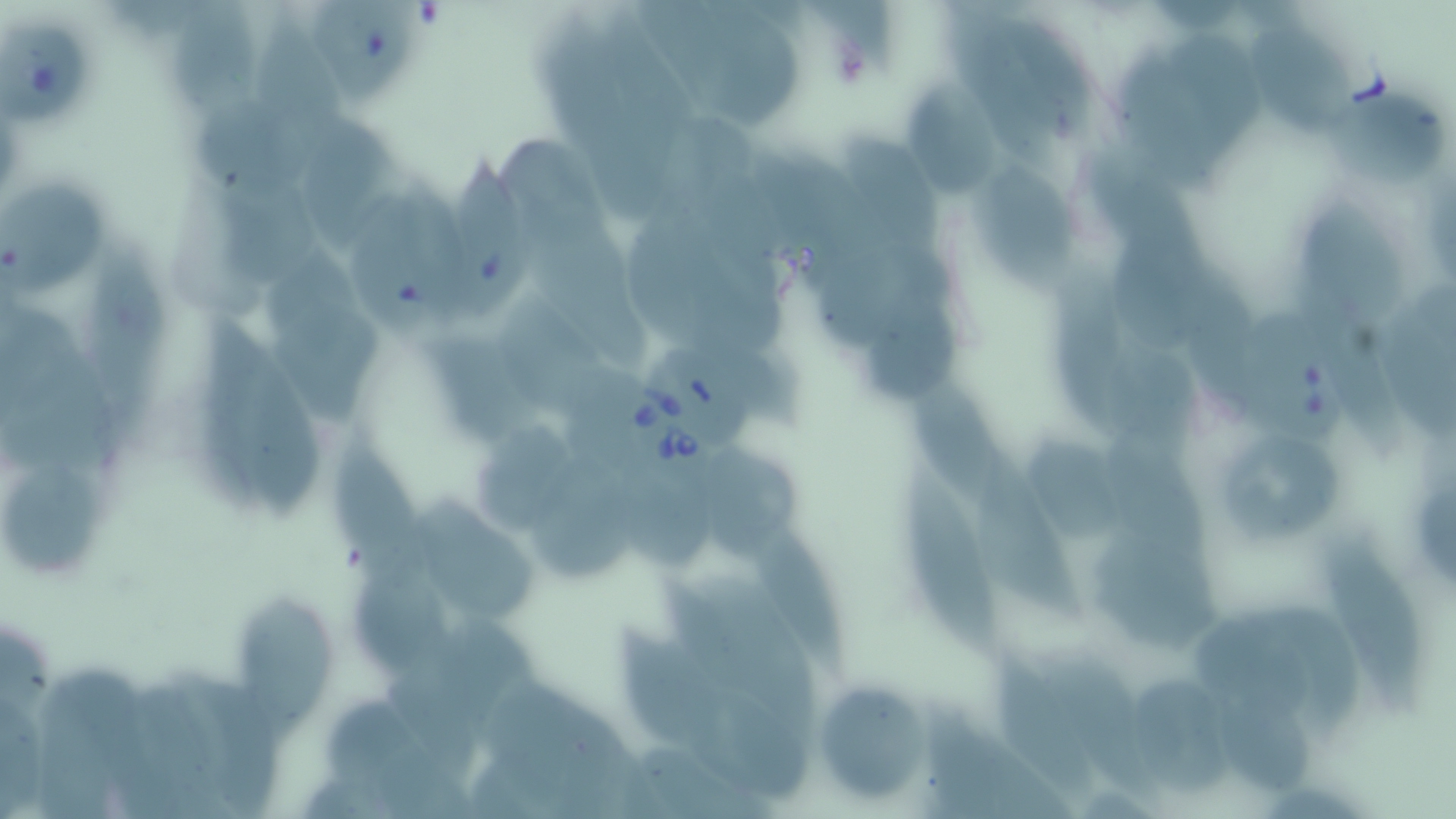
Approximate bounding boxes as named x1/y1/x2/y2 corners in pixels. Babesia divergens-infected red blood cell locations: (x1=1234, y1=298, x2=1353, y2=445), (x1=626, y1=357, x2=728, y2=503). Uninfected red blood cell locations: (x1=314, y1=1, x2=416, y2=107), (x1=174, y1=3, x2=260, y2=116), (x1=1244, y1=21, x2=1353, y2=135), (x1=1, y1=24, x2=90, y2=123), (x1=1164, y1=32, x2=1266, y2=156), (x1=1116, y1=51, x2=1225, y2=195), (x1=905, y1=83, x2=1008, y2=203), (x1=1324, y1=90, x2=1443, y2=185), (x1=300, y1=120, x2=395, y2=251), (x1=843, y1=133, x2=947, y2=258), (x1=972, y1=152, x2=1075, y2=289), (x1=444, y1=156, x2=527, y2=313), (x1=3, y1=180, x2=108, y2=296), (x1=1296, y1=201, x2=1408, y2=334), (x1=1103, y1=221, x2=1214, y2=354), (x1=82, y1=242, x2=164, y2=424), (x1=865, y1=287, x2=958, y2=399), (x1=495, y1=293, x2=616, y2=427), (x1=275, y1=304, x2=390, y2=424), (x1=420, y1=338, x2=532, y2=445), (x1=235, y1=353, x2=321, y2=518), (x1=917, y1=383, x2=1033, y2=520), (x1=472, y1=420, x2=583, y2=534), (x1=333, y1=432, x2=435, y2=593), (x1=1223, y1=436, x2=1345, y2=538), (x1=519, y1=446, x2=649, y2=585), (x1=712, y1=450, x2=807, y2=564), (x1=975, y1=452, x2=1090, y2=622), (x1=898, y1=466, x2=996, y2=650), (x1=3, y1=468, x2=104, y2=575), (x1=418, y1=493, x2=540, y2=625), (x1=1098, y1=532, x2=1215, y2=650), (x1=756, y1=534, x2=856, y2=687), (x1=1329, y1=535, x2=1423, y2=709), (x1=351, y1=569, x2=461, y2=678), (x1=239, y1=596, x2=340, y2=744), (x1=609, y1=617, x2=729, y2=757), (x1=996, y1=650, x2=1099, y2=800), (x1=1052, y1=656, x2=1177, y2=810), (x1=1133, y1=668, x2=1243, y2=800), (x1=1219, y1=675, x2=1317, y2=799), (x1=811, y1=679, x2=929, y2=805). Platelet locations: (x1=835, y1=45, x2=873, y2=86). Slide-level diagnosis: Babesia divergens. Light microscopy. May-Grünwald-Giemsa stain. One field of a larger specimen. Image is 1456×819 pixels. 1000x magnification. Thin blood film.